Identify the blood parasite species.
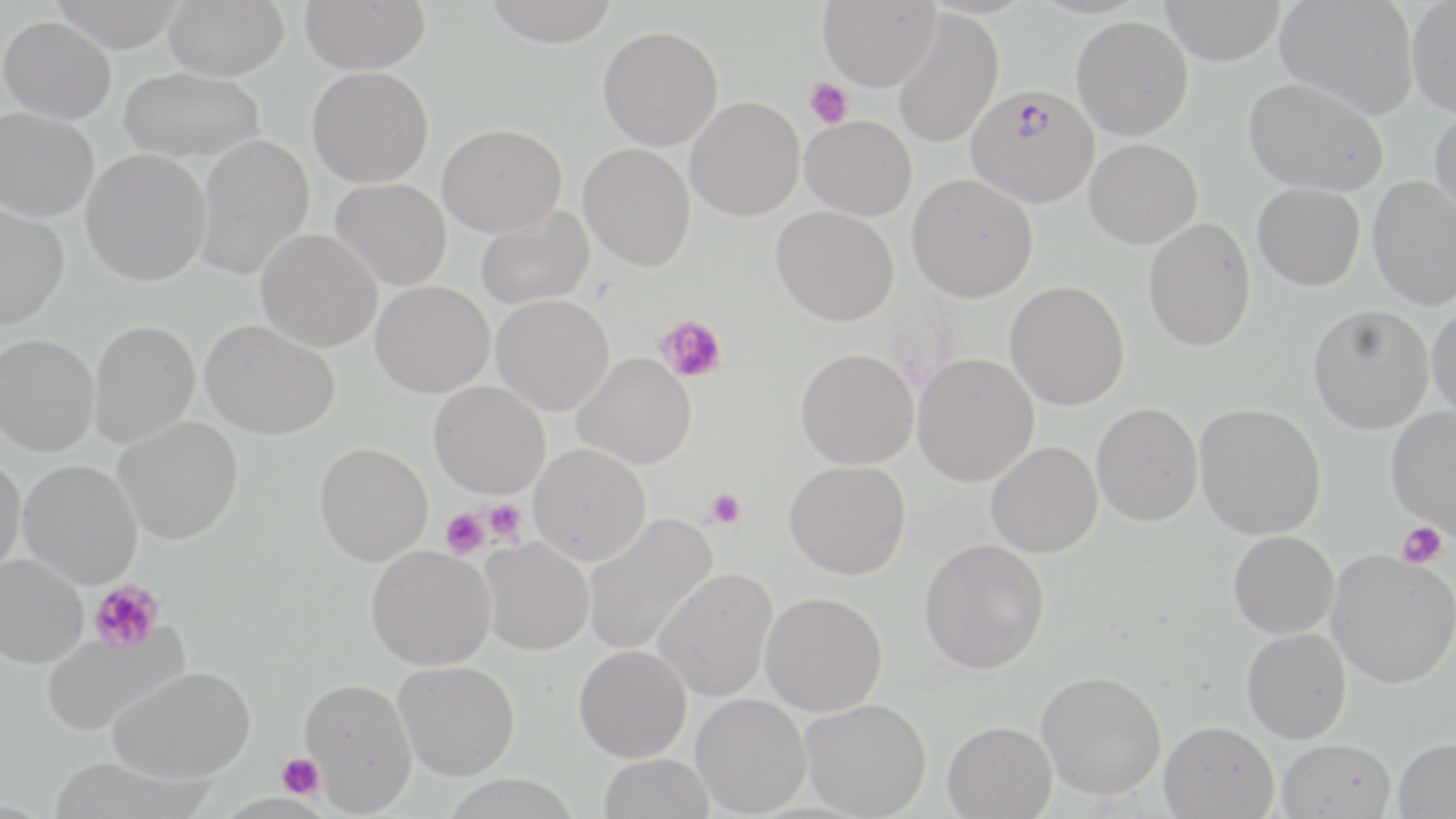
Plasmodium falciparum.

image size = 1456×819 pixels
Plasmodium falciparum-infected red blood cell locations = approximate bounding boxes as named x1/y1/x2/y2 corners in pixels: (x1=966, y1=85, x2=1099, y2=207)
magnification = 1000x
modality = optical microscopy
field of view = one of a larger specimen
uninfected red blood cell locations = approximate bounding boxes as named x1/y1/x2/y2 corners in pixels: (x1=48, y1=0, x2=188, y2=53), (x1=163, y1=0, x2=288, y2=80), (x1=300, y1=0, x2=430, y2=74), (x1=481, y1=0, x2=620, y2=48), (x1=817, y1=0, x2=940, y2=91), (x1=1160, y1=0, x2=1286, y2=65), (x1=1276, y1=0, x2=1418, y2=118), (x1=1407, y1=1, x2=1456, y2=118), (x1=891, y1=10, x2=1003, y2=149), (x1=0, y1=16, x2=116, y2=124), (x1=1072, y1=16, x2=1193, y2=140), (x1=597, y1=26, x2=723, y2=150), (x1=307, y1=66, x2=433, y2=188), (x1=118, y1=67, x2=265, y2=162), (x1=1244, y1=78, x2=1388, y2=196), (x1=685, y1=96, x2=805, y2=221), (x1=0, y1=107, x2=99, y2=222), (x1=1430, y1=107, x2=1456, y2=222), (x1=800, y1=115, x2=916, y2=220), (x1=437, y1=124, x2=566, y2=237), (x1=195, y1=135, x2=314, y2=279), (x1=1084, y1=139, x2=1202, y2=248), (x1=578, y1=143, x2=695, y2=271), (x1=81, y1=148, x2=211, y2=286), (x1=907, y1=174, x2=1038, y2=303), (x1=1368, y1=176, x2=1456, y2=310), (x1=330, y1=178, x2=452, y2=291), (x1=1252, y1=183, x2=1365, y2=291), (x1=0, y1=204, x2=69, y2=329), (x1=475, y1=206, x2=594, y2=309), (x1=771, y1=206, x2=899, y2=327), (x1=1144, y1=218, x2=1256, y2=352), (x1=255, y1=229, x2=382, y2=352), (x1=1005, y1=280, x2=1130, y2=410), (x1=370, y1=281, x2=494, y2=398), (x1=491, y1=294, x2=614, y2=416), (x1=1428, y1=300, x2=1456, y2=422), (x1=1308, y1=305, x2=1434, y2=433), (x1=200, y1=319, x2=339, y2=440), (x1=88, y1=320, x2=201, y2=448), (x1=0, y1=334, x2=99, y2=456), (x1=795, y1=348, x2=919, y2=469), (x1=571, y1=352, x2=695, y2=470), (x1=912, y1=353, x2=1039, y2=486), (x1=429, y1=381, x2=550, y2=499), (x1=1092, y1=403, x2=1202, y2=527), (x1=1194, y1=403, x2=1327, y2=540), (x1=1386, y1=407, x2=1456, y2=535), (x1=113, y1=417, x2=243, y2=544), (x1=986, y1=441, x2=1102, y2=558), (x1=314, y1=442, x2=433, y2=566), (x1=529, y1=443, x2=651, y2=565), (x1=0, y1=454, x2=26, y2=578), (x1=18, y1=460, x2=142, y2=589), (x1=784, y1=460, x2=911, y2=579), (x1=582, y1=512, x2=718, y2=657), (x1=1228, y1=530, x2=1339, y2=638), (x1=479, y1=538, x2=594, y2=655), (x1=919, y1=538, x2=1050, y2=675), (x1=366, y1=545, x2=496, y2=670), (x1=1326, y1=550, x2=1456, y2=689), (x1=0, y1=553, x2=88, y2=668), (x1=653, y1=568, x2=777, y2=702), (x1=760, y1=592, x2=888, y2=716), (x1=40, y1=624, x2=188, y2=734), (x1=1242, y1=627, x2=1351, y2=743), (x1=574, y1=644, x2=692, y2=762), (x1=394, y1=660, x2=520, y2=781), (x1=109, y1=666, x2=255, y2=783), (x1=1036, y1=670, x2=1166, y2=800), (x1=300, y1=677, x2=417, y2=813), (x1=691, y1=694, x2=811, y2=816), (x1=801, y1=698, x2=931, y2=819), (x1=942, y1=720, x2=1057, y2=818), (x1=1159, y1=720, x2=1279, y2=819), (x1=1392, y1=737, x2=1456, y2=818), (x1=1277, y1=739, x2=1396, y2=819), (x1=598, y1=753, x2=715, y2=819)
preparation = thin blood film
stain = May-Grünwald-Giemsa
platelet locations = approximate bounding boxes as named x1/y1/x2/y2 corners in pixels: (x1=805, y1=78, x2=853, y2=128), (x1=656, y1=313, x2=727, y2=384), (x1=705, y1=488, x2=747, y2=530), (x1=483, y1=499, x2=527, y2=544), (x1=442, y1=508, x2=489, y2=558), (x1=1397, y1=521, x2=1448, y2=568), (x1=89, y1=580, x2=164, y2=654), (x1=276, y1=754, x2=325, y2=799)